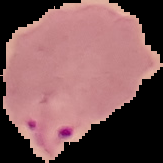
From a thin blood smear. Malaria status: parasitized. Segmented cell region on a black background. Image is 163×163 pixels.